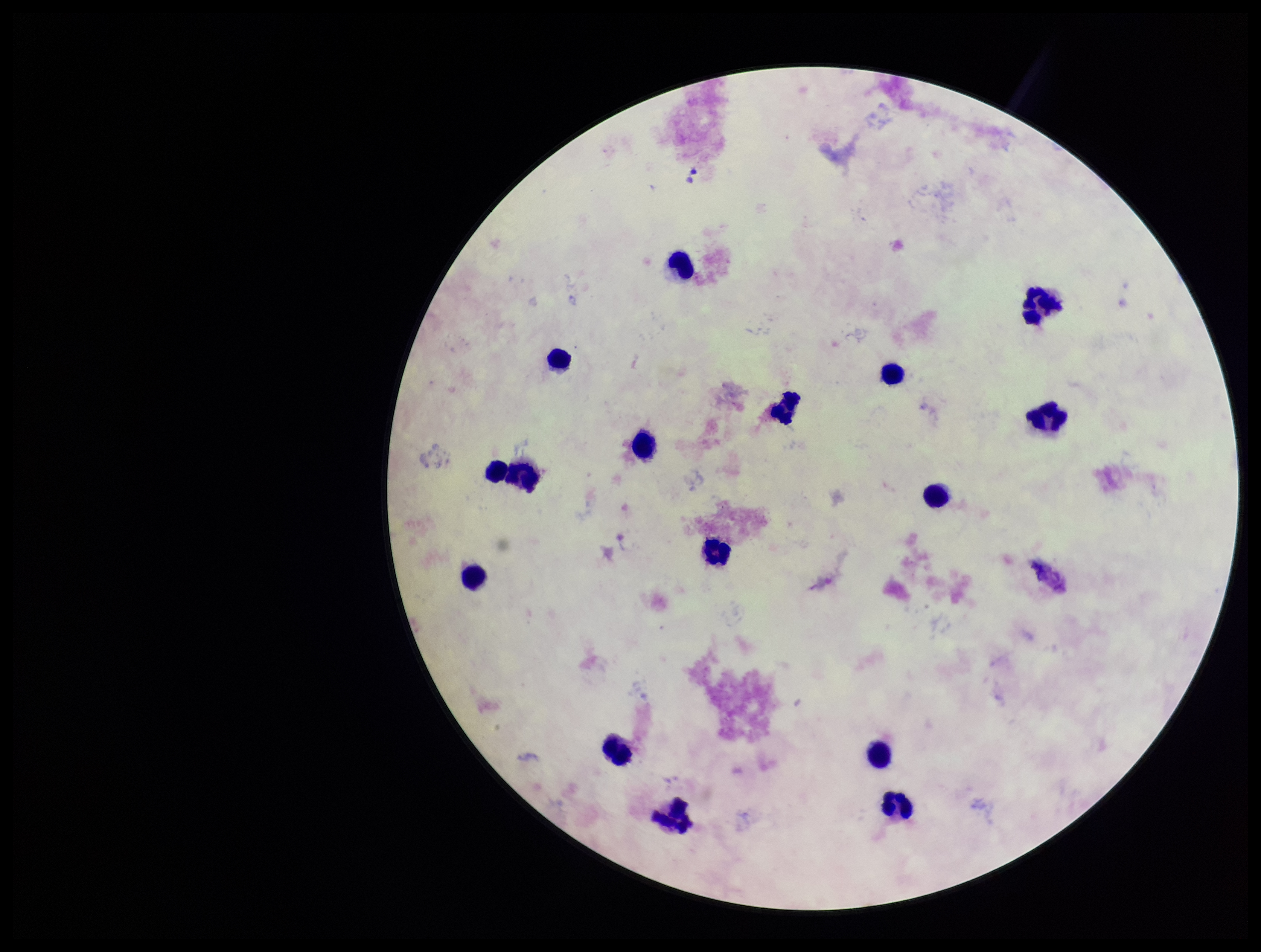

Summary:
  - Parasite count: 0
  - Patient malaria status: negative
  - Capture: smartphone photograph through the microscope eyepiece
  - Image size: 1261×952 pixels
  - Field of view: single
  - Preparation: thick blood smear
  - Leukocyte count: 16
  - Stain: Giemsa
  - Plasmodium parasites: none seen